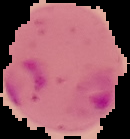
Summary:
  - Image type: segmented cell region on a black background
  - Preparation: thin blood film
  - Image size: 130×139 pixels
  - Result: Plasmodium parasites detected